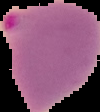 Result: Plasmodium parasites detected. From a thin blood film. Image is 100×112 pixels. The area outside the segmented cell region is set to black.